Classify this cell by malaria status.
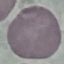
Uninfected.

Summary:
  - Stain: Giemsa
  - Image type: cell patch, automatically extracted from a larger field of view and resized to 64 × 64 pixels
  - Capture: smartphone through the microscope eyepiece
  - Preparation: thin blood film